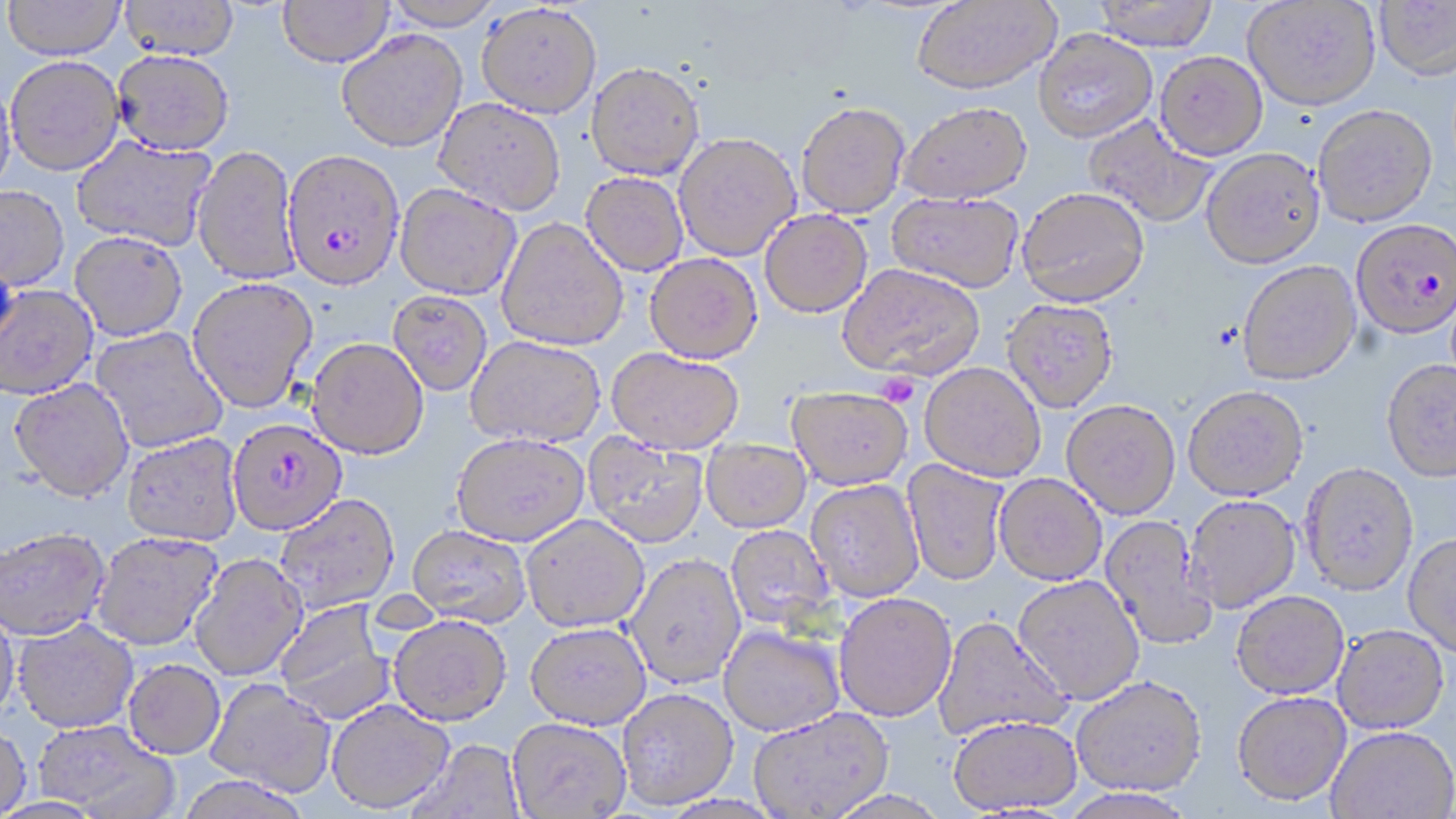
slide-level diagnosis = Plasmodium falciparum
platelet locations = approximate bounding boxes as (x1,y1)-(x2,y2) corner pairs in pixels: (876,372)-(920,408)
stain = May-Grünwald-Giemsa
image size = 1456×819 pixels
uninfected red blood cell locations = approximate bounding boxes as (x1,y1)-(x2,y2) corner pairs in pixels: (3,0)-(126,59), (119,0)-(239,59), (277,0)-(394,67), (381,0)-(503,30), (912,0)-(1061,95), (1093,0)-(1220,50), (1243,1)-(1381,111), (1375,1)-(1456,80), (476,3)-(601,119), (337,29)-(467,153), (1034,29)-(1157,142), (112,49)-(235,154), (1155,51)-(1268,160), (5,55)-(125,176), (586,62)-(705,181), (0,76)-(17,200), (433,97)-(566,217), (796,102)-(910,219), (898,102)-(1032,205), (1312,104)-(1438,227), (1084,116)-(1217,229), (673,133)-(801,261), (71,135)-(216,251), (192,145)-(300,286), (1201,147)-(1326,269), (581,172)-(688,276), (395,183)-(521,301), (0,185)-(70,292), (1017,186)-(1150,308), (887,192)-(1024,293), (759,209)-(872,318), (496,219)-(628,352), (69,232)-(188,342), (644,254)-(763,365), (1237,260)-(1361,384), (837,263)-(985,381), (187,277)-(317,414), (0,284)-(99,400), (388,291)-(493,397), (1001,299)-(1119,413), (90,326)-(229,453), (466,336)-(606,450), (306,339)-(428,461), (606,349)-(743,456), (1381,359)-(1456,481), (919,362)-(1046,483), (8,378)-(134,503), (1183,385)-(1309,501), (786,386)-(913,491), (1061,400)-(1180,520), (121,433)-(243,547), (583,433)-(708,549), (451,435)-(589,548), (701,438)-(811,533), (902,459)-(1010,587), (1300,462)-(1419,595), (994,474)-(1107,586), (805,479)-(925,602), (274,494)-(400,614), (1183,495)-(1301,613), (521,515)-(650,634), (1100,515)-(1217,651), (725,525)-(835,631), (406,526)-(532,628), (0,528)-(111,642), (91,532)-(223,651), (1402,534)-(1456,656), (189,554)-(308,681), (625,554)-(747,689), (1013,575)-(1145,704), (1231,591)-(1350,699), (834,593)-(958,722), (274,598)-(394,725), (0,603)-(20,726), (388,615)-(512,727), (932,616)-(1071,744), (12,619)-(139,734), (524,623)-(651,731), (1333,624)-(1449,733), (718,625)-(844,738), (123,660)-(225,760), (1071,675)-(1207,797), (204,678)-(337,797), (617,688)-(739,811), (1232,692)-(1351,806), (326,699)-(455,814), (747,708)-(894,818), (948,715)-(1083,815), (507,718)-(631,818), (32,720)-(178,818), (0,725)-(32,818), (1327,726)-(1456,819), (408,740)-(527,819), (176,776)-(313,819), (1059,788)-(1198,818), (824,790)-(951,819)
Plasmodium falciparum-infected red blood cell locations = approximate bounding boxes as (x1,y1)-(x2,y2) corner pairs in pixels: (282,150)-(405,292), (1350,218)-(1456,337), (226,418)-(346,538)
field of view = one of a larger specimen
preparation = thin blood smear
modality = optical microscopy
magnification = 1000x